Assess this cell for malaria.
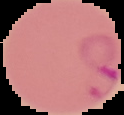
It is parasitized.

Summary:
  - Image size: 124×115 pixels
  - Preparation: thin blood smear
  - Image type: segmented cell region on a black background